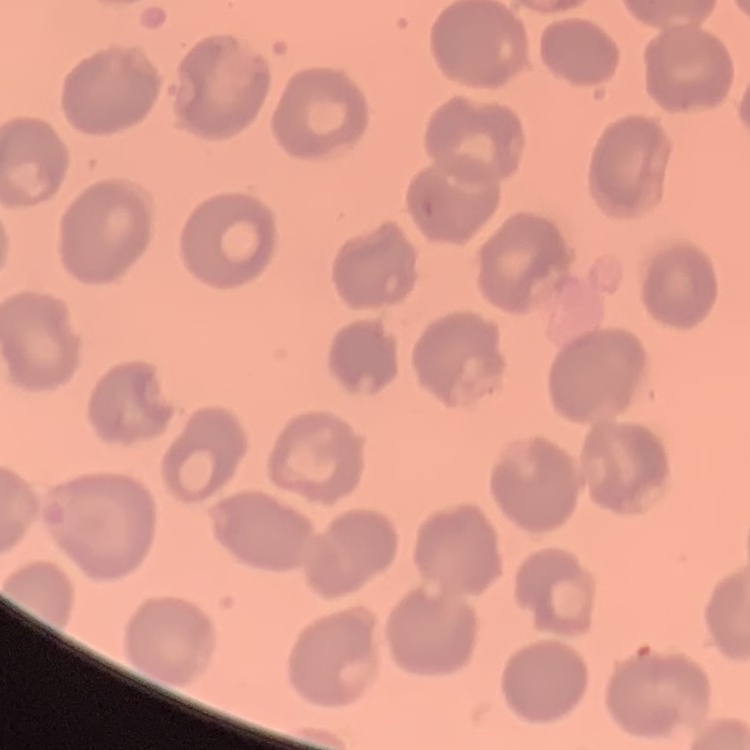

erythrocyte_morphology: no rouleaux formation
preparation: thin blood smear
image_type: square crop of a larger photomicrograph
stain: Field's or Giemsa